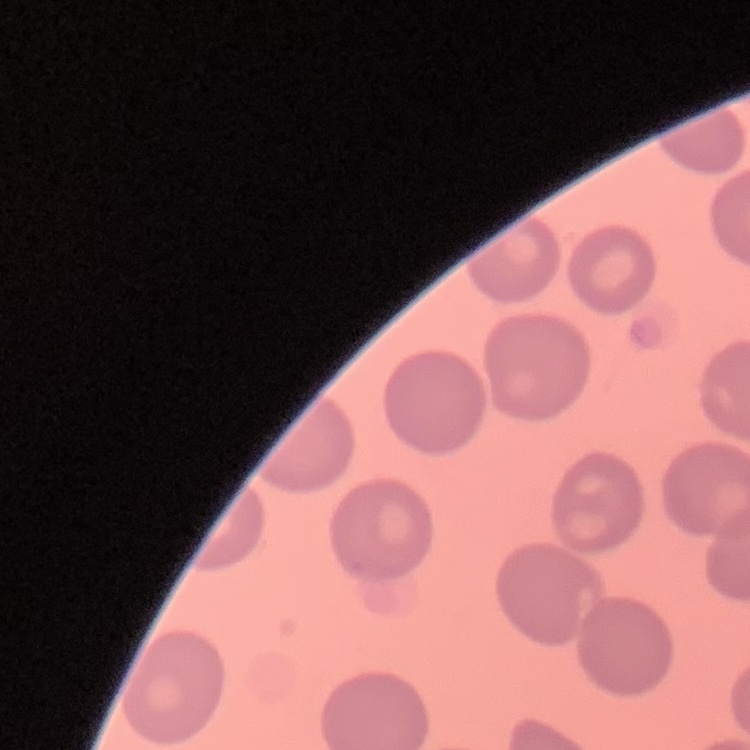

red blood cell morphology = no rouleaux formation
image type = square crop of a larger photomicrograph
stain = Field's or Giemsa
preparation = thin blood film